Classify this cell by malaria status.
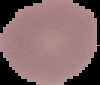

Uninfected.

Segmented cell region on a black background. Image is 100×85 pixels. From a thin blood smear.